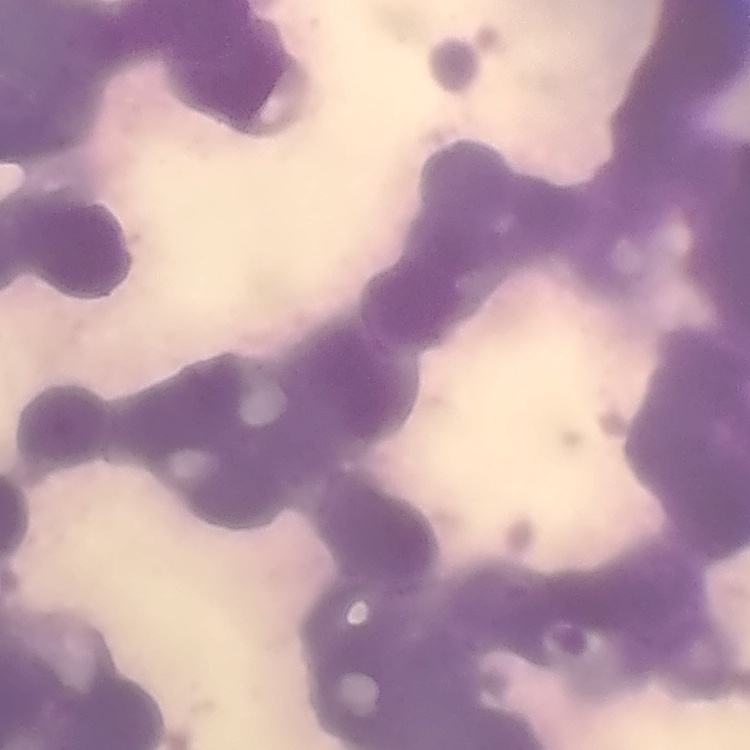

erythrocyte_morphology: rouleaux formation
stain: Field's or Giemsa
preparation: thin blood film
image_type: one tile cut from a larger photomicrograph